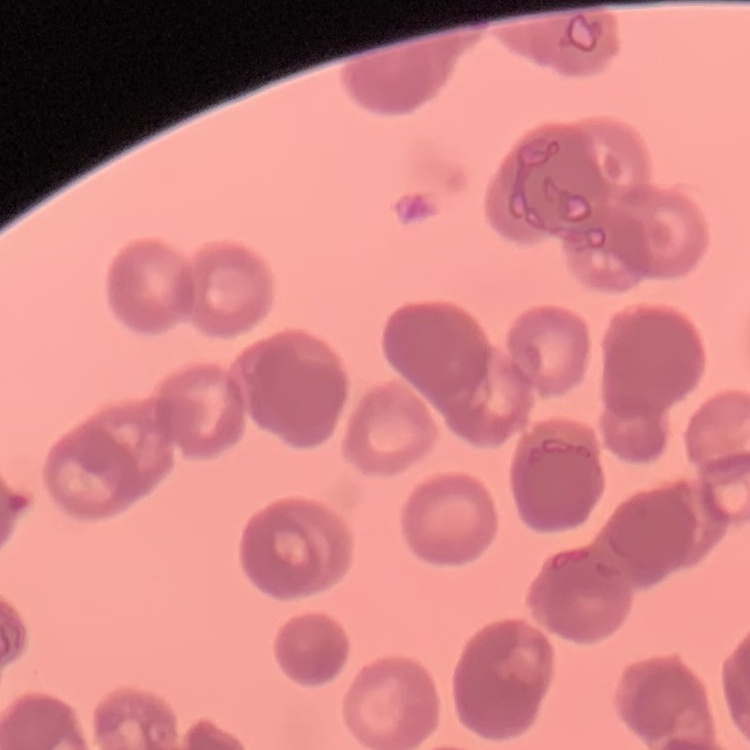

Summary:
  - Red blood cell morphology: rouleaux formation
  - Stain: Field's or Giemsa
  - Image type: one tile cut from a larger photomicrograph
  - Preparation: thin blood smear